Give the extent of all Plasmodium falciparum-infected red blood cells.
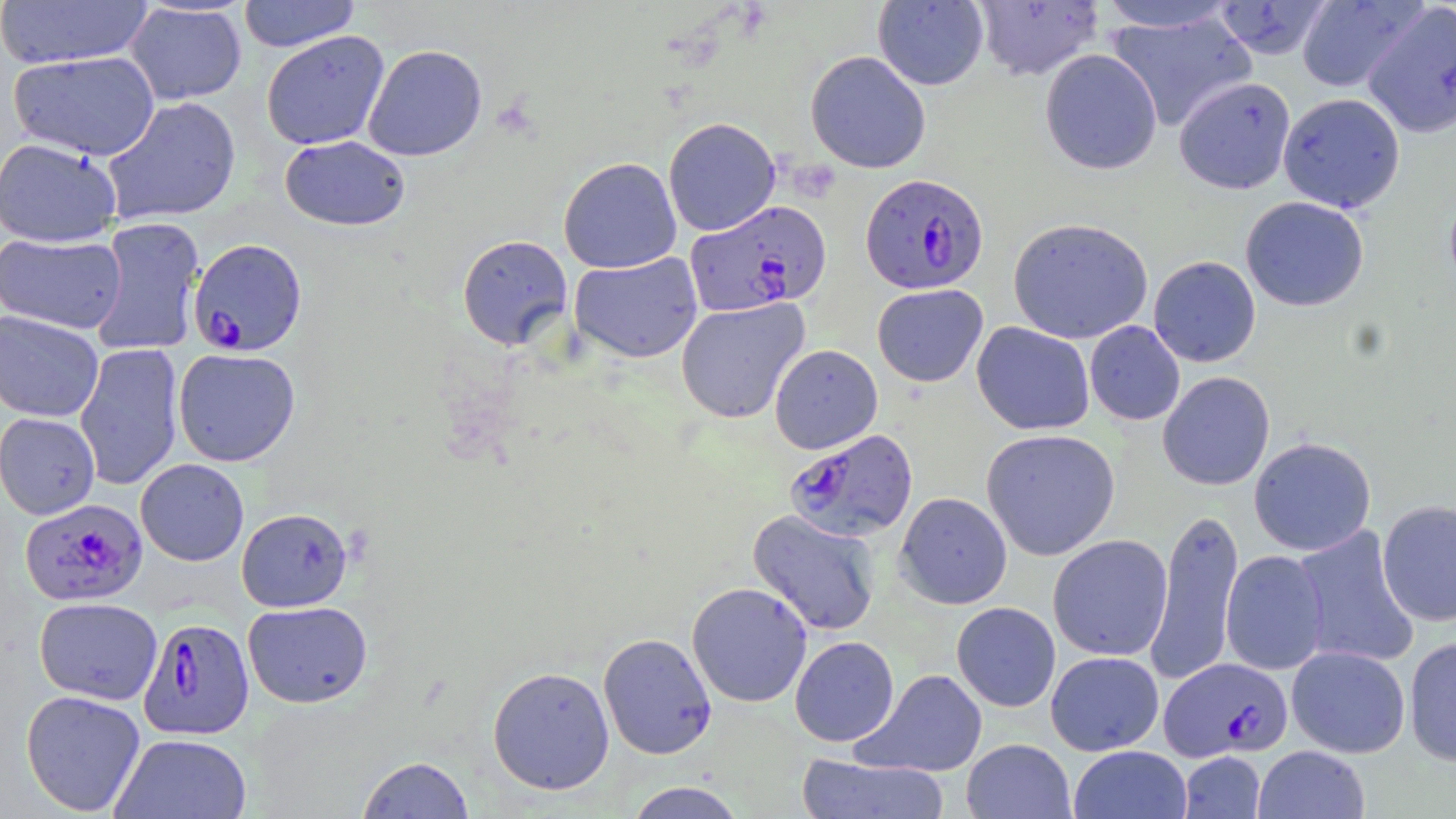
Approximate bounding boxes as (x1,y1)-(x2,y2) corner pairs in pixels.
Plasmodium falciparum-infected red blood cells: (860,172)-(989,294), (685,200)-(831,316), (189,238)-(307,357), (785,428)-(919,542), (20,498)-(148,606), (138,617)-(255,739), (1160,657)-(1293,760).

slide-level diagnosis = Plasmodium falciparum
uninfected red blood cell locations = approximate bounding boxes as (x1,y1)-(x2,y2) corner pairs in pixels: (238,0)-(361,52), (972,0)-(1105,81), (1294,0)-(1424,92), (0,1)-(153,69), (872,1)-(989,90), (1094,1)-(1240,32), (1211,1)-(1333,60), (125,2)-(247,105), (1363,3)-(1456,138), (1106,11)-(1257,132), (260,30)-(391,150), (362,44)-(487,161), (1040,49)-(1162,174), (8,50)-(160,161), (805,50)-(931,173), (1174,76)-(1296,194), (1277,92)-(1405,213), (102,96)-(241,224), (663,117)-(781,236), (279,135)-(410,231), (0,137)-(123,248), (558,156)-(681,273), (1443,185)-(1456,300), (1240,196)-(1369,312), (88,216)-(206,356), (1007,217)-(1154,344), (0,232)-(127,334), (457,234)-(573,351), (569,252)-(703,363), (1148,256)-(1261,367), (872,284)-(988,387), (676,298)-(810,423), (0,310)-(104,422), (971,321)-(1095,435), (1084,321)-(1185,426), (74,342)-(184,491), (769,344)-(883,454), (173,348)-(300,466), (1157,371)-(1275,490), (0,412)-(100,519), (981,428)-(1120,561), (1249,436)-(1376,556), (135,459)-(249,566), (895,492)-(1012,609), (1377,499)-(1456,627), (236,507)-(353,612), (1145,507)-(1244,685), (748,509)-(882,637), (1293,526)-(1420,669), (1048,534)-(1173,661), (1220,550)-(1329,675), (687,582)-(812,708), (34,597)-(163,705), (243,600)-(372,708), (951,602)-(1060,712), (598,632)-(717,760), (790,636)-(899,746), (1404,636)-(1456,765), (1287,645)-(1411,758), (1045,651)-(1164,756), (487,665)-(615,795), (855,668)-(988,777), (20,689)-(146,816), (110,733)-(252,819), (961,738)-(1076,818), (1069,745)-(1193,819), (1253,745)-(1370,819), (1179,751)-(1266,818), (796,753)-(949,819), (357,756)-(476,818), (623,781)-(748,818)
image size = 1456×819 pixels
preparation = thin blood smear
field of view = single
magnification = 1000x
stain = May-Grünwald-Giemsa
modality = optical microscopy